Outline each blood parasite and name the species.
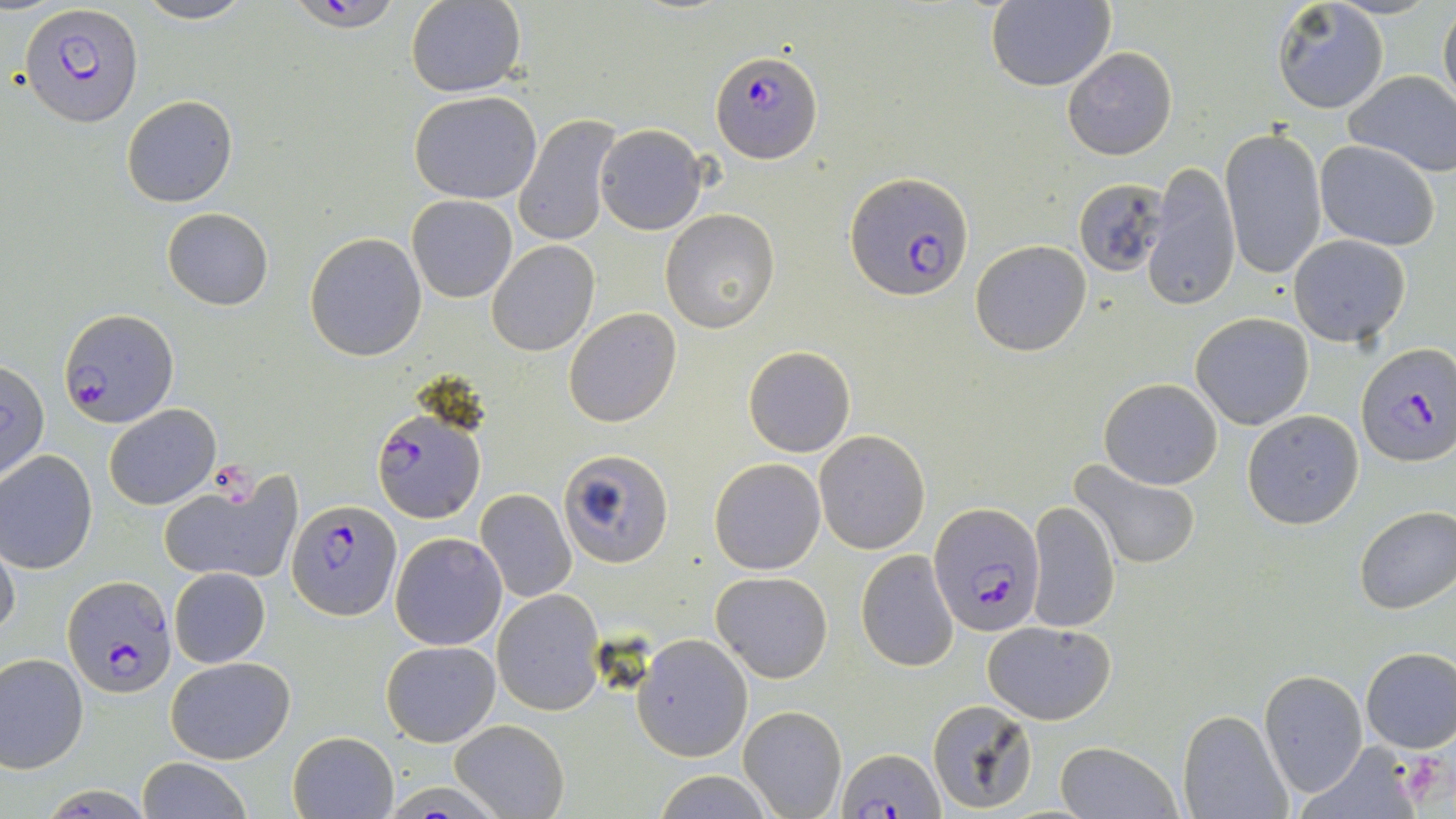
Approximate bounding boxes as [x1, y1, x2, y2] in pixels.
Plasmodium falciparum-infected red blood cells: [294, 0, 398, 37], [22, 3, 143, 127], [711, 51, 824, 164], [846, 173, 976, 303], [61, 308, 178, 427], [1356, 344, 1455, 466], [371, 406, 485, 521], [289, 500, 401, 619], [931, 500, 1044, 636], [63, 575, 178, 697], [841, 747, 943, 817].
No Plasmodium ovale, Plasmodium malariae, Plasmodium vivax, Babesia divergens, or Trypanosoma brucei observed.

slide-level diagnosis = Plasmodium falciparum
stain = May-Grünwald-Giemsa
field of view = single
magnification = 1000x
preparation = thin blood smear
platelet locations = approximate bounding boxes as [x1, y1, x2, y2] in pixels: [212, 460, 260, 506], [1406, 753, 1451, 797]
image size = 1456×819 pixels
modality = optical microscopy
uninfected red blood cell locations = approximate bounding boxes as [x1, y1, x2, y2] in pixels: [130, 0, 257, 26], [406, 0, 526, 98], [1273, 0, 1389, 115], [985, 1, 1115, 93], [1439, 1, 1456, 119], [1063, 47, 1177, 160], [1344, 70, 1456, 178], [408, 91, 542, 205], [121, 95, 237, 207], [514, 114, 624, 249], [594, 125, 706, 235], [1220, 127, 1327, 278], [1315, 140, 1440, 251], [1144, 163, 1240, 310], [1073, 177, 1170, 278], [407, 195, 517, 303], [162, 208, 274, 310], [660, 210, 778, 332], [304, 232, 427, 361], [1288, 234, 1411, 348], [486, 239, 599, 356], [970, 240, 1091, 355], [564, 307, 681, 427], [1190, 313, 1314, 429], [743, 346, 856, 458], [0, 362, 49, 481], [1099, 377, 1222, 489], [104, 403, 220, 510], [1242, 410, 1365, 529], [813, 429, 930, 554], [558, 448, 675, 567], [0, 450, 99, 575], [709, 457, 826, 574], [1069, 460, 1202, 570], [158, 470, 302, 588], [476, 489, 577, 603], [1027, 502, 1119, 634], [1354, 505, 1456, 615], [390, 532, 506, 650], [0, 536, 21, 641], [856, 549, 959, 673], [169, 567, 271, 668], [712, 571, 833, 683], [493, 588, 605, 716], [982, 620, 1116, 725], [632, 635, 752, 761], [381, 639, 500, 746], [1359, 646, 1456, 753], [0, 653, 89, 771], [165, 655, 295, 764], [1258, 670, 1368, 795], [926, 698, 1038, 815], [738, 705, 846, 818], [1178, 710, 1291, 819], [449, 719, 569, 819], [288, 731, 398, 818], [1055, 741, 1180, 819], [1299, 742, 1424, 817], [136, 758, 254, 818], [655, 771, 776, 817]